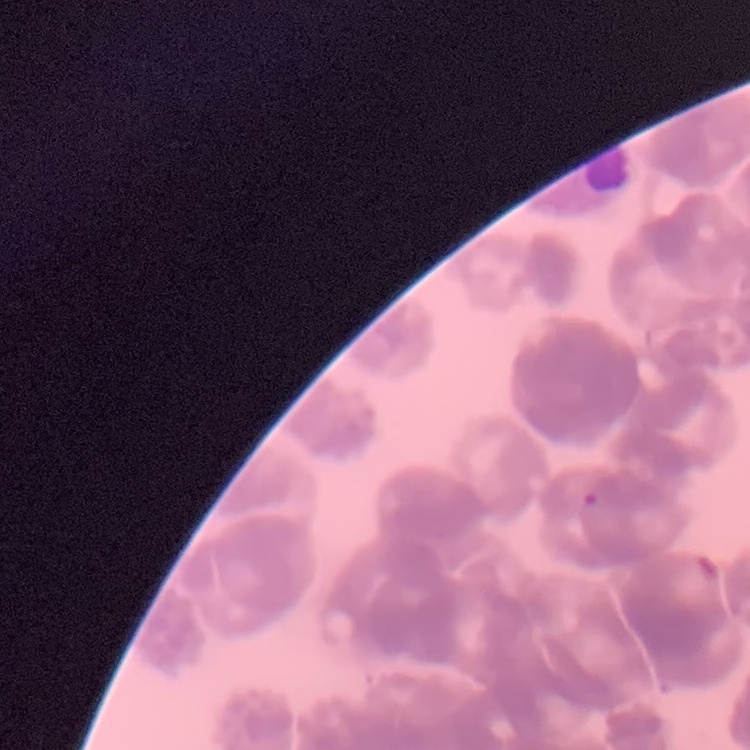
red_blood_cell_morphology: rouleaux formation
preparation: thin blood film
stain: Field's or Giemsa
image_type: one tile cut from a larger photomicrograph